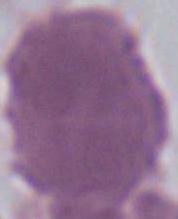

Summary:
  - Modality: micrograph
  - Identification: erythrocyte
  - Magnification: 1000x